State which parasite is depicted.
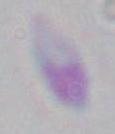

Toxoplasma gondii.

Summary:
  - Magnification: 1000x
  - Modality: photomicrograph